Outline each uninfected red blood cell.
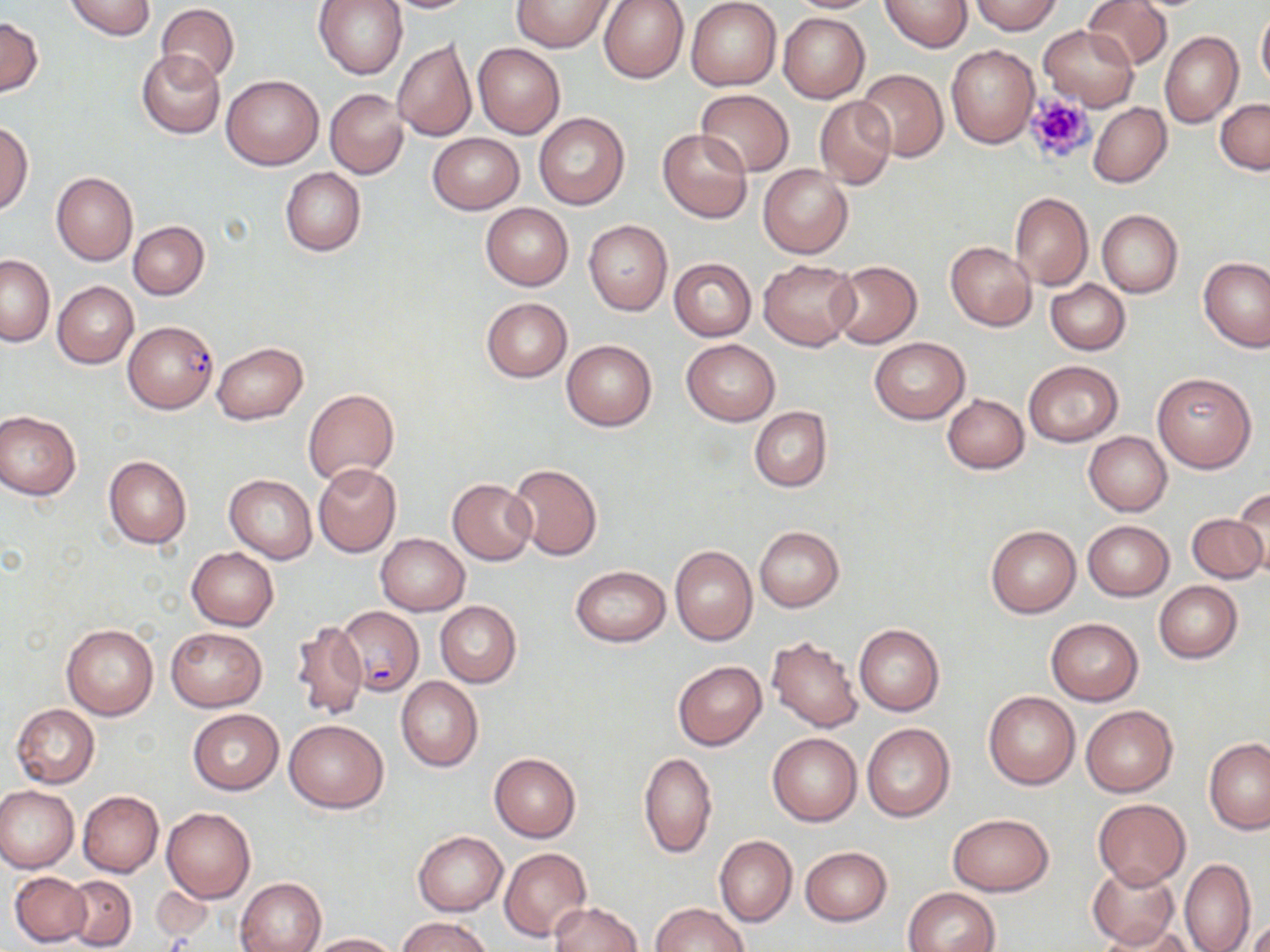
Approximate bounding boxes as (x1, y1, x2, y2) in pixels.
Uninfected red blood cells: (63, 0, 158, 41), (313, 0, 408, 79), (381, 0, 474, 12), (511, 0, 613, 52), (599, 0, 688, 83), (687, 0, 782, 89), (786, 0, 883, 13), (880, 0, 973, 52), (972, 0, 1060, 35), (1083, 0, 1173, 70), (514, 1, 687, 65), (155, 4, 239, 86), (1256, 8, 1270, 90), (778, 12, 870, 103), (0, 16, 43, 96), (1038, 24, 1139, 110), (1160, 31, 1242, 128), (393, 40, 477, 141), (472, 43, 565, 138), (945, 45, 1039, 150), (135, 50, 225, 139), (857, 68, 947, 162), (221, 75, 324, 169), (325, 88, 409, 179), (694, 89, 793, 176), (816, 95, 896, 188), (1215, 98, 1270, 174), (1089, 103, 1172, 188), (534, 113, 629, 210), (1, 121, 32, 213), (657, 127, 752, 223), (429, 132, 523, 214), (758, 164, 852, 258), (280, 167, 366, 257), (51, 172, 138, 265), (1010, 193, 1093, 289), (481, 203, 573, 290), (1097, 209, 1183, 297), (128, 220, 209, 299), (584, 220, 673, 315), (945, 241, 1036, 331), (1, 254, 54, 345), (669, 258, 756, 341), (1200, 258, 1270, 352), (759, 259, 860, 351), (829, 261, 921, 349), (1046, 279, 1130, 354), (53, 280, 138, 369), (481, 298, 571, 382), (870, 338, 969, 423), (561, 339, 657, 431), (682, 339, 779, 424), (213, 343, 307, 423), (1023, 360, 1123, 446), (1152, 371, 1256, 473), (303, 389, 399, 484), (942, 394, 1029, 473), (749, 406, 831, 492), (0, 410, 81, 500), (1084, 432, 1172, 516), (103, 455, 192, 549), (508, 462, 602, 560), (313, 463, 402, 558), (225, 474, 317, 563), (447, 478, 536, 565), (1232, 484, 1270, 575), (1186, 513, 1267, 584), (1083, 520, 1174, 600), (985, 525, 1081, 617), (754, 526, 844, 611), (375, 534, 469, 616), (670, 546, 757, 645), (186, 548, 278, 631), (569, 565, 670, 645), (1154, 581, 1243, 662), (435, 601, 521, 687), (290, 618, 369, 722), (1046, 618, 1143, 705), (61, 623, 159, 720), (854, 623, 944, 715), (167, 627, 266, 711), (767, 634, 864, 732), (672, 661, 766, 750), (396, 677, 484, 772), (984, 691, 1080, 789), (11, 704, 100, 789), (1081, 706, 1178, 796), (187, 709, 283, 795), (284, 718, 388, 812), (862, 722, 956, 822), (767, 732, 861, 826), (1204, 738, 1270, 834), (638, 752, 717, 859), (489, 753, 581, 841), (0, 785, 78, 873), (77, 791, 163, 877), (1093, 799, 1189, 888), (162, 806, 256, 903), (947, 813, 1054, 896), (413, 831, 507, 915), (714, 836, 796, 926), (800, 846, 892, 925), (499, 847, 592, 941), (1178, 857, 1255, 952), (1087, 862, 1179, 948), (10, 872, 90, 947), (63, 876, 136, 950), (236, 877, 326, 952), (153, 886, 217, 941), (904, 887, 1000, 952), (551, 902, 642, 952), (650, 902, 748, 952), (1242, 913, 1269, 952), (398, 917, 492, 952), (1097, 921, 1197, 952), (307, 933, 401, 951).

slide_level_diagnosis: Plasmodium falciparum
modality: light microscopy
platelet_locations: 'approximate bounding boxes as (x1, y1, x2, y2) in pixels: (1022, 93, 1098, 165)'
stain: May-Grünwald-Giemsa
field_of_view: single
magnification: 1000x
plasmodium_falciparum_infected_red_blood_cell_locations: 'approximate bounding boxes as (x1, y1, x2, y2) in pixels: (124, 321, 217, 414), (337, 605, 423, 697)'
image_size: 1270×952 pixels
preparation: thin blood smear